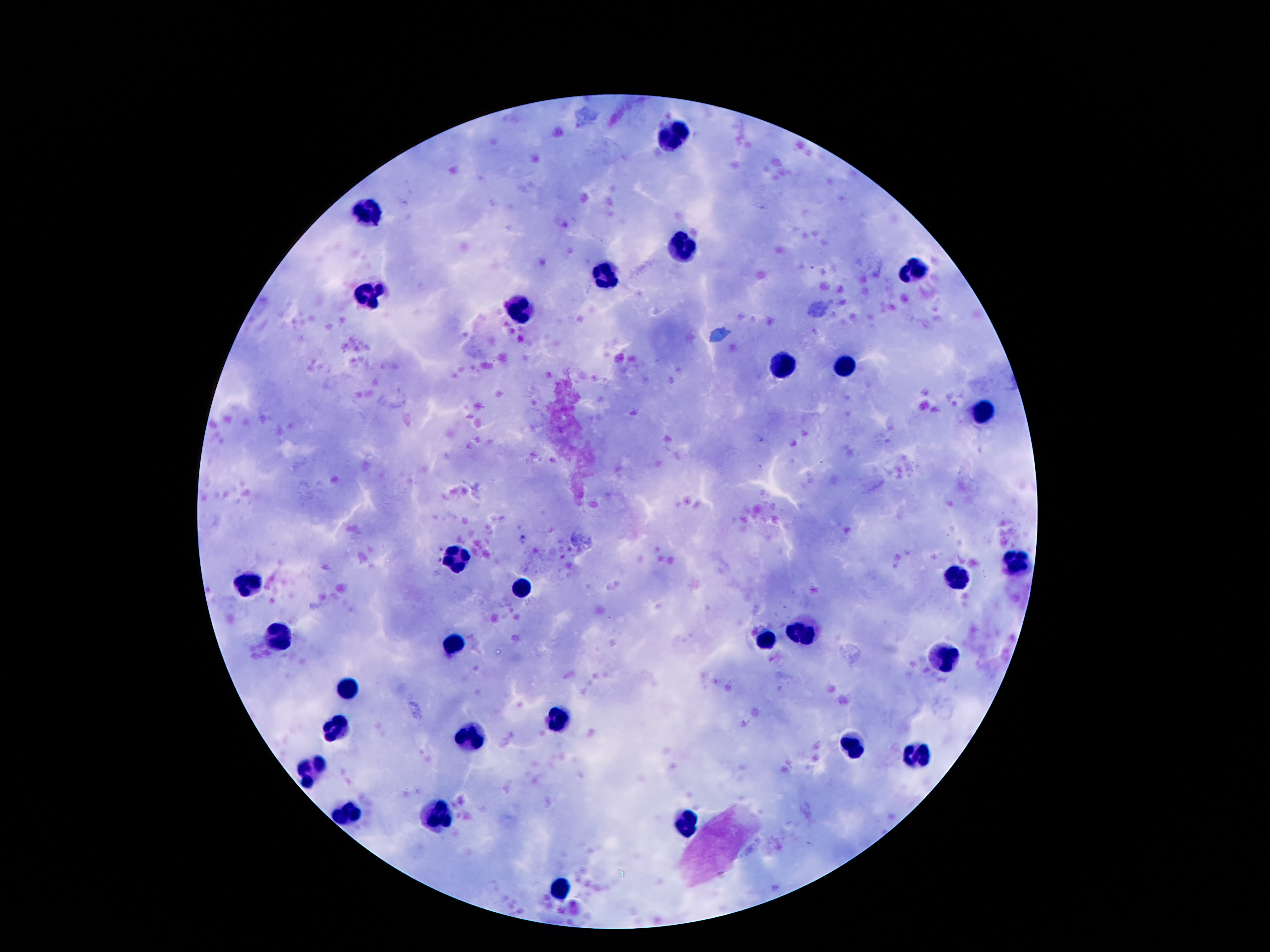
field of view = single
stain = Giemsa
patient malaria status = uninfected
magnification = 100x
capture = smartphone camera through the microscope eyepiece
image size = 1270×952 pixels
preparation = thick blood smear
leukocyte locations = approximate centers as (x, y) in pixels: (673, 135), (367, 210), (681, 248), (913, 268), (605, 274), (370, 295), (521, 311), (781, 365), (843, 366), (982, 416), (458, 555), (1017, 563), (956, 578), (247, 580), (523, 587), (806, 632), (281, 637), (765, 643), (451, 644), (943, 657), (347, 688), (558, 720), (337, 725), (470, 739), (853, 745), (915, 753), (312, 768), (347, 817), (437, 819), (685, 821), (562, 893)